Report the malaria status of this cell.
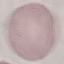

Uninfected.

Thin blood film. Cell patch, automatically extracted from a larger field of view and resized to 64 × 64 pixels. Photographed with a smartphone camera at the microscope eyepiece. Giemsa stain.